State the blood parasite species.
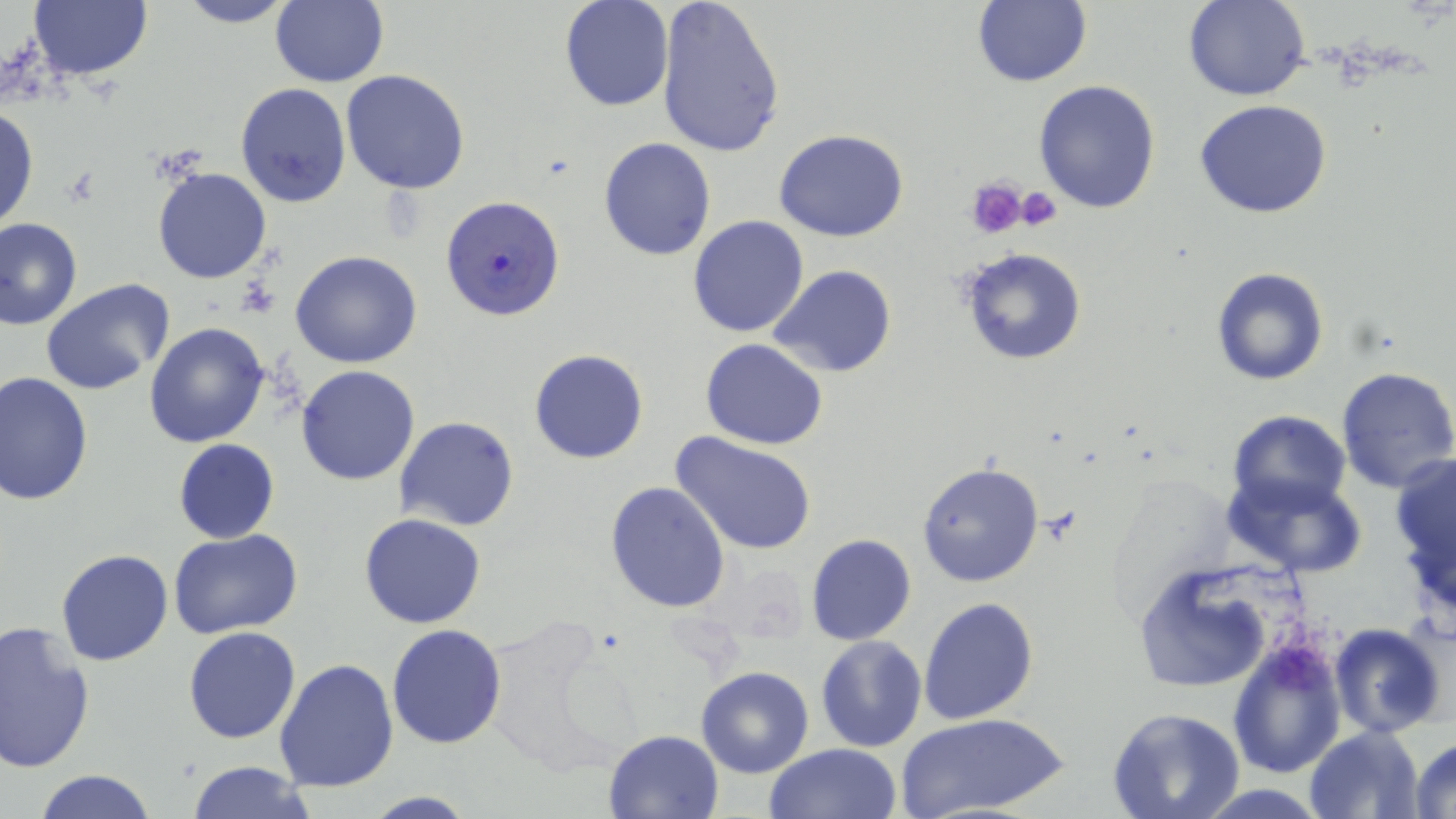
Plasmodium falciparum.

Approximate bounding boxes as named x1/y1/x2/y2 corners in pixels. Platelet locations: (x1=964, y1=175, x2=1028, y2=238), (x1=1012, y1=184, x2=1063, y2=231). Plasmodium falciparum-infected red blood cell locations: (x1=441, y1=195, x2=564, y2=321). Uninfected red blood cell locations: (x1=174, y1=0, x2=298, y2=27), (x1=269, y1=0, x2=388, y2=89), (x1=559, y1=0, x2=673, y2=112), (x1=656, y1=0, x2=787, y2=159), (x1=971, y1=0, x2=1092, y2=87), (x1=1185, y1=0, x2=1310, y2=101), (x1=28, y1=2, x2=153, y2=82), (x1=340, y1=69, x2=471, y2=194), (x1=1033, y1=80, x2=1162, y2=214), (x1=236, y1=82, x2=352, y2=210), (x1=1194, y1=100, x2=1333, y2=220), (x1=1, y1=104, x2=38, y2=233), (x1=774, y1=129, x2=911, y2=243), (x1=598, y1=136, x2=715, y2=260), (x1=152, y1=166, x2=272, y2=284), (x1=687, y1=215, x2=811, y2=338), (x1=1, y1=218, x2=83, y2=330), (x1=959, y1=246, x2=1087, y2=365), (x1=290, y1=250, x2=423, y2=368), (x1=767, y1=265, x2=897, y2=380), (x1=1211, y1=267, x2=1328, y2=386), (x1=38, y1=281, x2=174, y2=395), (x1=144, y1=322, x2=272, y2=449), (x1=700, y1=339, x2=830, y2=450), (x1=529, y1=349, x2=649, y2=464), (x1=296, y1=365, x2=420, y2=485), (x1=1335, y1=367, x2=1456, y2=494), (x1=0, y1=373, x2=95, y2=504), (x1=1227, y1=410, x2=1351, y2=517), (x1=394, y1=417, x2=520, y2=532), (x1=669, y1=431, x2=817, y2=555), (x1=173, y1=438, x2=280, y2=544), (x1=1391, y1=455, x2=1456, y2=616), (x1=916, y1=460, x2=1044, y2=589), (x1=1223, y1=470, x2=1367, y2=577), (x1=604, y1=481, x2=731, y2=613), (x1=358, y1=514, x2=486, y2=630), (x1=170, y1=530, x2=302, y2=641), (x1=805, y1=534, x2=916, y2=646), (x1=56, y1=549, x2=173, y2=665), (x1=1133, y1=563, x2=1281, y2=693), (x1=919, y1=596, x2=1039, y2=724), (x1=0, y1=619, x2=97, y2=775), (x1=1329, y1=624, x2=1447, y2=739), (x1=386, y1=625, x2=507, y2=749), (x1=184, y1=626, x2=301, y2=744), (x1=814, y1=636, x2=928, y2=753), (x1=1228, y1=639, x2=1344, y2=777), (x1=273, y1=658, x2=400, y2=792), (x1=696, y1=667, x2=814, y2=778), (x1=1107, y1=704, x2=1245, y2=819), (x1=898, y1=712, x2=1067, y2=819), (x1=1304, y1=726, x2=1424, y2=818), (x1=604, y1=728, x2=725, y2=818), (x1=1409, y1=736, x2=1456, y2=817), (x1=763, y1=742, x2=904, y2=819), (x1=185, y1=761, x2=317, y2=818), (x1=31, y1=769, x2=160, y2=819), (x1=360, y1=791, x2=480, y2=818). Image is 1456×819 pixels. Single field of view. May-Grünwald-Giemsa stain. Thin blood film. Optical microscopy. Captured at 1000x magnification.